Outline each blood parasite and name the species.
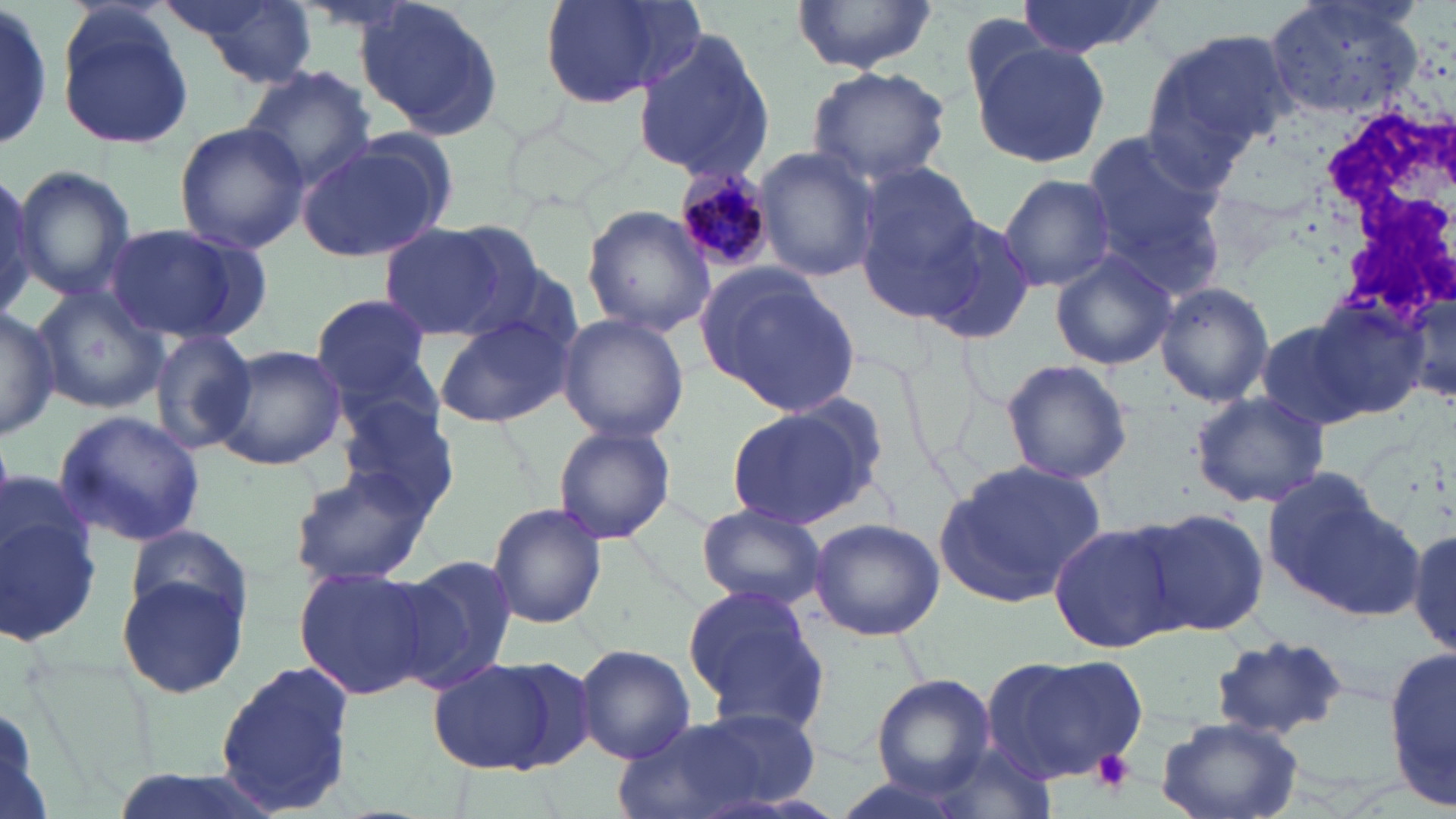
Approximate bounding boxes as (x1,y1)-(x2,y2) corner pairs in pixels.
Plasmodium malariae-infected red blood cells: (676,165)-(775,273).
No Plasmodium falciparum, Plasmodium ovale, Plasmodium vivax, Babesia divergens, or Trypanosoma brucei observed.

{
  "slide_level_diagnosis": "Plasmodium malariae",
  "platelet_locations": "approximate bounding boxes as (x1,y1)-(x2,y2) corner pairs in pixels: (1090,748)-(1135,795)",
  "image_size": "1456×819 pixels",
  "white_blood_cell_locations": "approximate bounding boxes as (x1,y1)-(x2,y2) corner pairs in pixels: (1303,76)-(1454,319)",
  "modality": "light microscopy",
  "field_of_view": "one of a larger specimen",
  "stain": "May-Grünwald-Giemsa",
  "uninfected_red_blood_cell_locations": "approximate bounding boxes as (x1,y1)-(x2,y2) corner pairs in pixels: (171,0)-(319,85), (539,0)-(702,111), (790,0)-(940,73), (1012,0)-(1167,60), (1266,0)-(1422,123), (1,2)-(54,155), (356,2)-(507,140), (56,11)-(193,152), (630,29)-(774,182), (1140,29)-(1289,172), (971,40)-(1108,167), (807,64)-(954,188), (241,66)-(376,192), (174,122)-(307,253), (295,133)-(454,264), (1080,133)-(1229,281), (753,147)-(882,284), (12,165)-(136,301), (855,166)-(986,319), (0,173)-(43,318), (996,173)-(1117,292), (582,204)-(716,336), (915,215)-(1039,346), (101,222)-(268,347), (379,225)-(512,340), (1049,251)-(1177,372), (697,266)-(860,416), (1154,280)-(1275,407), (32,284)-(166,416), (1407,285)-(1455,407), (309,293)-(440,411), (1303,295)-(1432,419), (0,305)-(57,443), (556,313)-(690,442), (430,316)-(573,428), (1254,316)-(1381,433), (148,327)-(258,456), (212,344)-(345,469), (111,345)-(241,500), (998,358)-(1133,484), (1190,392)-(1329,509), (333,396)-(462,521), (722,404)-(879,531), (52,410)-(207,546), (553,424)-(676,545), (937,459)-(1105,609), (287,467)-(434,586), (1259,471)-(1418,619), (0,493)-(102,648), (486,501)-(608,629), (695,503)-(826,610), (1137,507)-(1272,636), (808,519)-(944,641), (123,522)-(253,635), (1048,522)-(1184,652), (1409,527)-(1455,654), (392,555)-(518,693), (294,564)-(438,700), (116,566)-(251,701), (682,584)-(826,724), (1203,636)-(1352,746), (1388,643)-(1456,812), (575,644)-(697,763), (981,653)-(1147,787), (426,654)-(578,776), (214,662)-(359,812), (872,675)-(995,796), (0,692)-(59,819), (614,713)-(805,819), (1154,715)-(1305,819), (922,740)-(1058,819), (104,768)-(285,819)",
  "preparation": "thin blood smear",
  "magnification": "1000x"
}